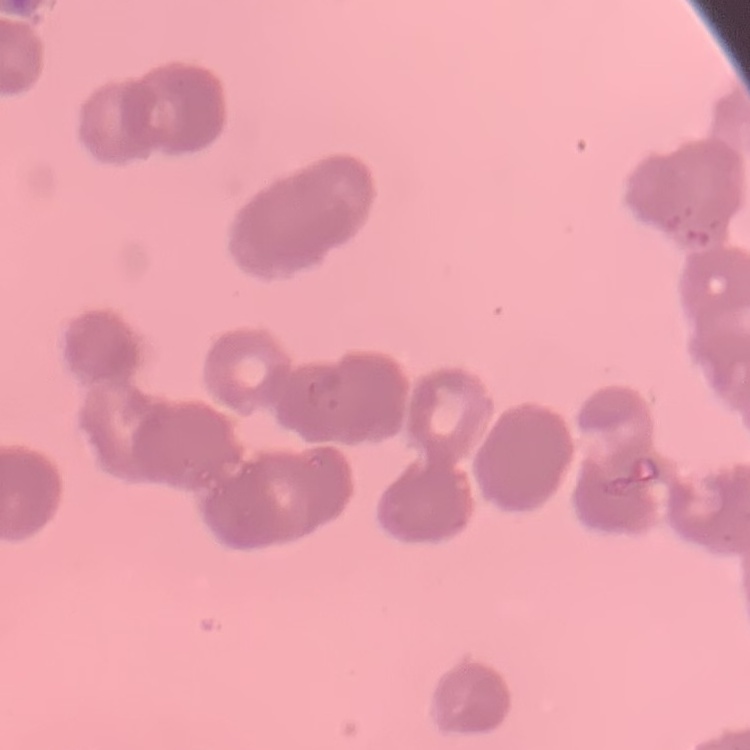
Summary:
  - Erythrocyte morphology: rouleaux formation
  - Stain: Field's or Giemsa
  - Preparation: thin blood smear
  - Image type: one tile cut from a larger photomicrograph